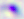 Photomicrograph. Captured at 400x magnification. Toxoplasma gondii is seen.